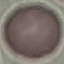
result = no malaria parasites detected
capture = smartphone through the microscope eyepiece
preparation = thin smear
stain = Giemsa
image type = automatically extracted cell patch, resized to 64 × 64 pixels